Locate every leukocyte (white blood cell).
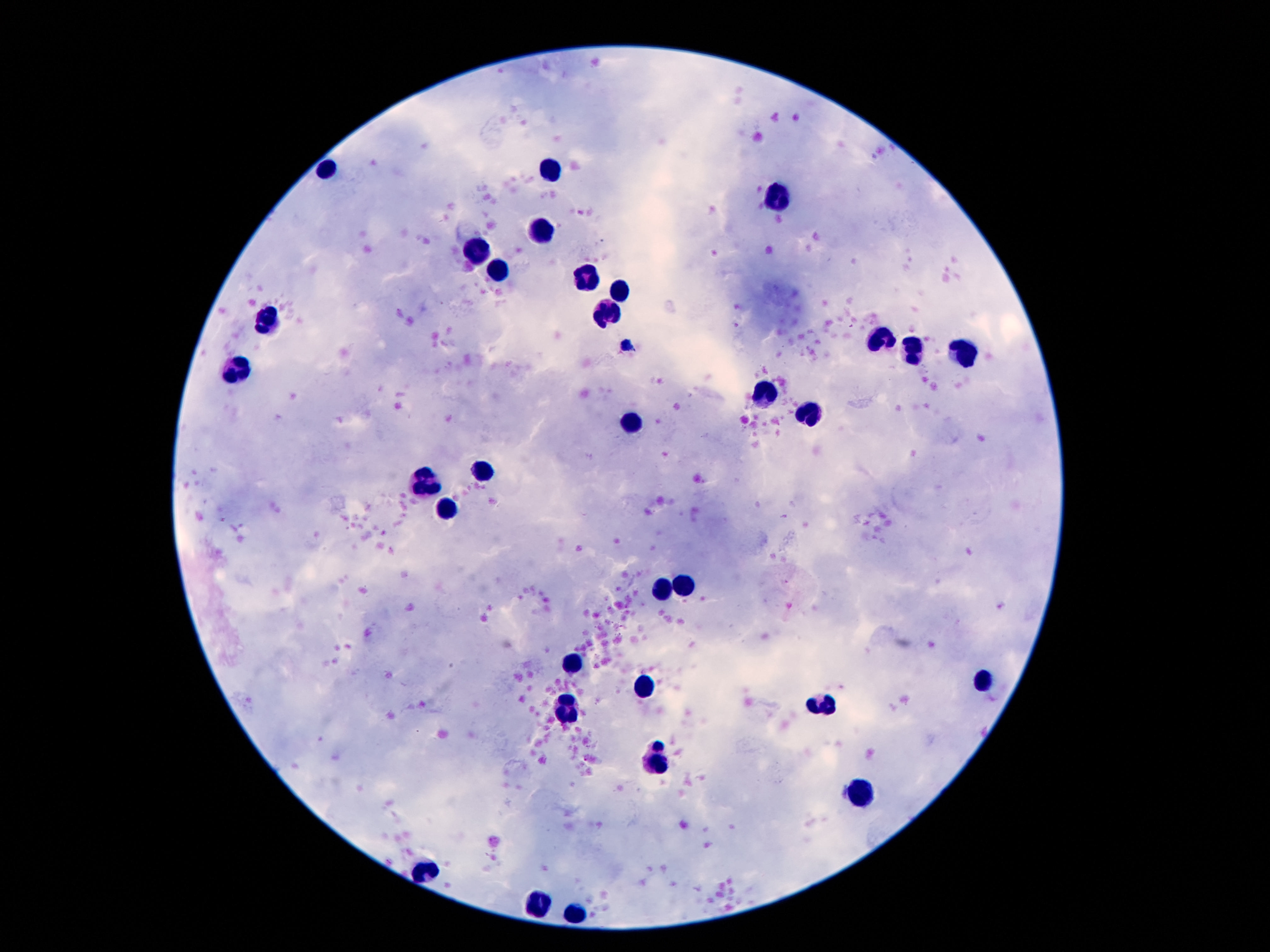

Approximate object centers, in pixels from the top-left corner.
Leukocytes: (x=329, y=166), (x=552, y=169), (x=786, y=201), (x=541, y=230), (x=478, y=253), (x=498, y=267), (x=588, y=274), (x=617, y=291), (x=610, y=313), (x=263, y=322), (x=879, y=338), (x=965, y=350), (x=912, y=351), (x=241, y=370), (x=766, y=394), (x=807, y=416), (x=630, y=419), (x=481, y=470), (x=432, y=487), (x=449, y=506), (x=665, y=587), (x=682, y=589), (x=576, y=659), (x=984, y=682), (x=646, y=688), (x=567, y=702), (x=821, y=704), (x=656, y=762), (x=860, y=791), (x=428, y=868), (x=540, y=903), (x=577, y=911).

Thick blood smear. Patient malaria status: not infected. 100x magnification. One field from this slide. Image is 1270×952 pixels. Giemsa stain. Photographed through the microscope eyepiece with a smartphone camera.